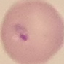 Result: malaria parasites detected. Giemsa-stained preparation. Acquired by smartphone through the microscope eyepiece. Automatically extracted cell patch, resized to 64 × 64 pixels. Thin smear of blood.